State the blood parasite species.
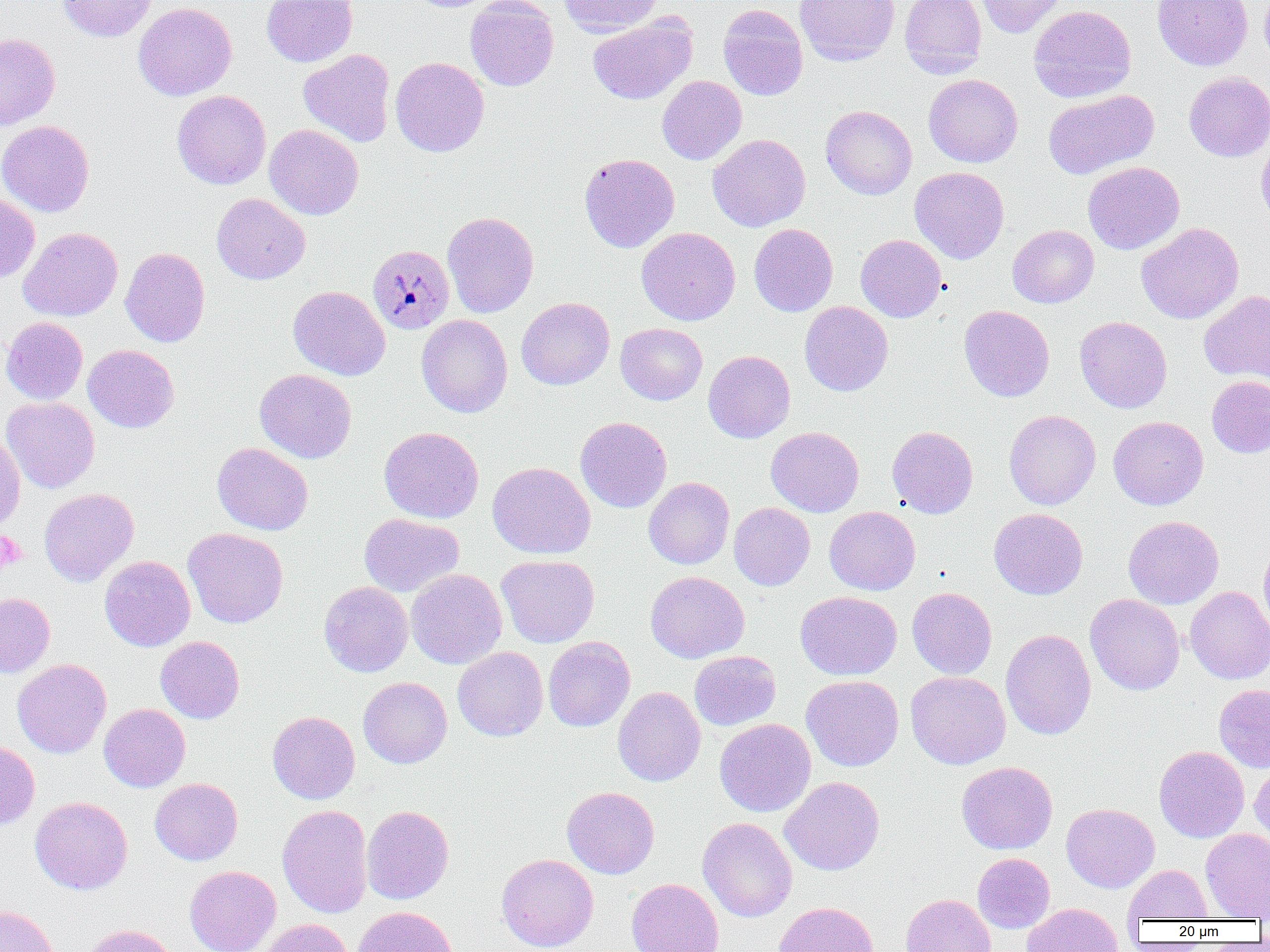
Plasmodium malariae.

Summary:
  - Coordinate format: approximate bounding boxes as (x1,y1)-(x2,y2) corner pairs in pixels
  - Plasmodium malariae-infected red blood cell locations: (368,244)-(454,334)
  - Uninfected red blood cell locations: (57,0)-(157,42), (262,0)-(357,67), (405,0)-(497,12), (465,0)-(559,91), (558,0)-(661,36), (795,0)-(899,65), (899,0)-(987,79), (976,0)-(1068,38), (1152,0)-(1253,70), (1260,0)-(1270,65), (133,2)-(237,100), (718,4)-(808,101), (1028,5)-(1136,103), (588,14)-(697,105), (0,33)-(60,130), (298,49)-(396,147), (391,56)-(489,157), (1184,71)-(1270,161), (923,74)-(1023,167), (657,75)-(747,165), (1043,89)-(1159,179), (172,90)-(271,189), (820,105)-(917,199), (0,120)-(94,216), (264,124)-(364,219), (707,134)-(811,232), (1256,135)-(1270,231), (579,153)-(680,252), (1083,161)-(1184,254), (910,167)-(1009,263), (212,193)-(310,284), (0,194)-(40,283), (442,211)-(539,318), (1137,222)-(1243,324), (749,223)-(838,316), (1007,224)-(1099,308), (19,227)-(122,321), (636,227)-(740,325), (855,234)-(946,322), (120,247)-(210,347), (288,286)-(390,380), (1199,290)-(1270,385), (516,297)-(615,389), (799,301)-(893,396), (959,305)-(1055,401), (416,314)-(512,417), (1075,316)-(1172,413), (0,317)-(88,404), (615,323)-(707,405), (83,344)-(179,433), (703,350)-(795,443), (254,368)-(356,463), (1206,376)-(1270,458), (2,396)-(99,493), (1004,410)-(1101,509), (575,416)-(672,513), (1108,416)-(1208,510), (379,426)-(484,523), (887,426)-(978,518), (766,427)-(864,516), (0,430)-(25,531), (212,442)-(313,535), (487,462)-(595,559), (644,477)-(734,569), (39,487)-(139,586), (729,502)-(815,590), (824,506)-(920,595), (989,508)-(1088,599), (360,513)-(464,596), (1123,516)-(1224,608), (183,527)-(288,628), (1258,535)-(1270,638), (496,554)-(599,647), (100,556)-(195,651), (406,568)-(507,669), (645,571)-(749,663), (319,581)-(413,677), (907,587)-(997,679), (1185,587)-(1270,684), (796,591)-(902,680), (0,593)-(55,677), (1085,593)-(1185,695), (1000,628)-(1096,740), (156,636)-(244,723), (543,637)-(635,731), (453,646)-(548,741), (689,650)-(781,730), (12,658)-(111,758), (905,671)-(1010,769), (801,675)-(904,771), (358,677)-(452,768), (1214,684)-(1270,773), (612,686)-(706,786), (99,704)-(190,791), (267,711)-(360,804), (714,718)-(816,817), (0,740)-(40,831), (1154,745)-(1249,842), (1250,759)-(1270,849), (957,761)-(1057,854), (779,776)-(884,875), (150,778)-(243,865), (562,786)-(659,879), (30,796)-(133,894), (1061,803)-(1159,892), (277,804)-(373,919), (361,805)-(454,904), (698,817)-(797,922), (1201,829)-(1270,920), (972,852)-(1055,932), (496,853)-(598,952), (184,865)-(281,952), (1124,865)-(1212,922), (626,878)-(723,952), (901,893)-(996,952), (773,901)-(879,952), (1022,902)-(1123,952), (0,904)-(59,952), (352,906)-(458,952), (256,918)-(354,952), (79,924)-(178,952)
  - Platelet locations: (1,532)-(25,569)
  - Modality: optical microscopy
  - Preparation: thin blood smear
  - Magnification: 1000x
  - Image size: 1270×952 pixels
  - Field of view: single